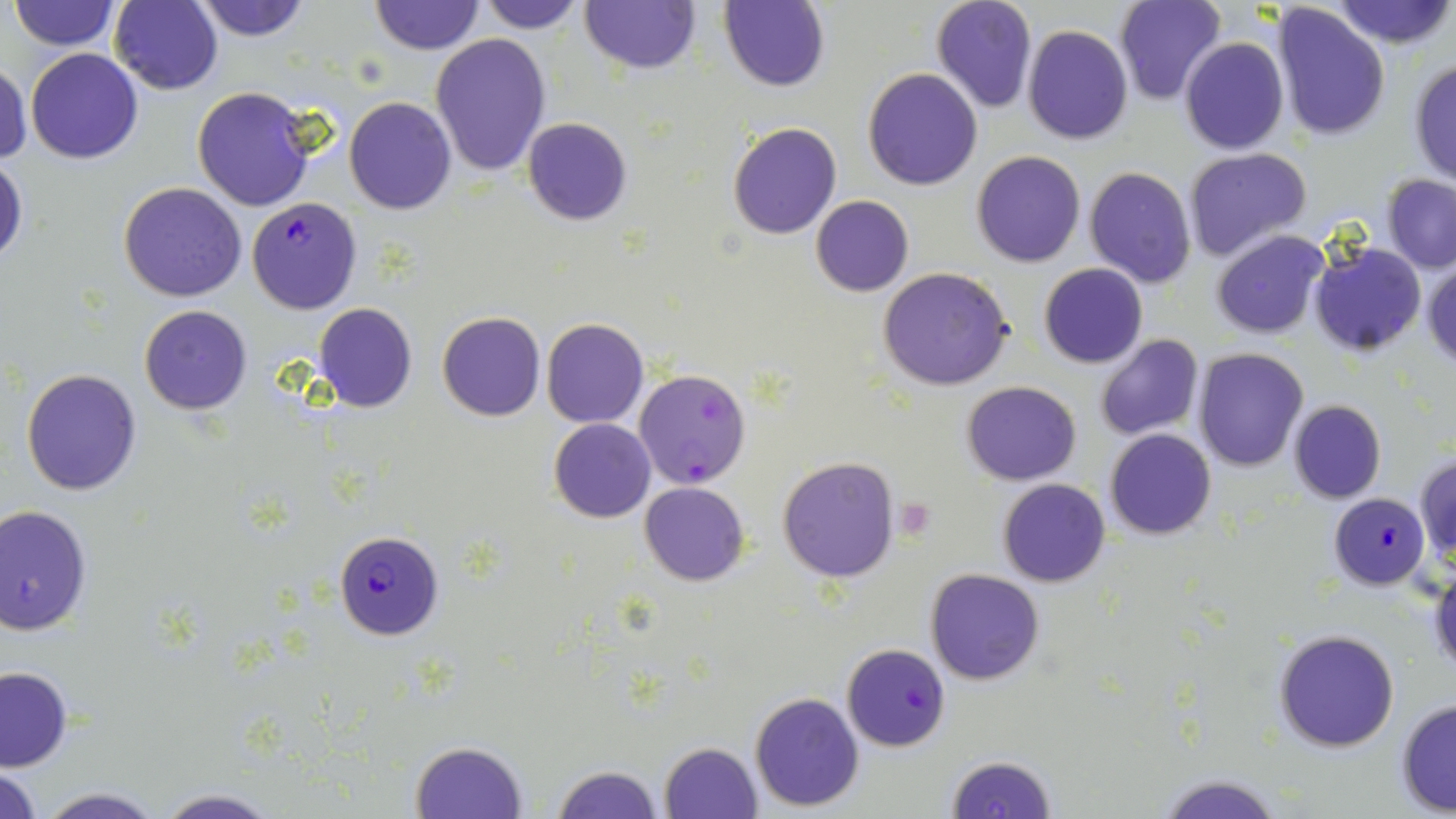
Approximate bounding boxes as (x1,y1)-(x2,y2) corner pairs in pixels. Plasmodium falciparum-infected red blood cell locations: (246,197)-(362,315), (633,368)-(751,490), (1329,492)-(1430,590), (334,531)-(443,640), (842,643)-(951,751). Platelet locations: (895,497)-(935,540). Uninfected red blood cell locations: (191,0)-(315,41), (580,0)-(700,73), (932,0)-(1038,114), (1115,0)-(1225,108), (1331,0)-(1456,50), (9,1)-(121,51), (109,1)-(222,94), (476,1)-(587,33), (720,1)-(830,91), (368,2)-(485,54), (1271,3)-(1392,142), (1022,23)-(1133,147), (429,34)-(550,178), (1180,36)-(1288,156), (25,48)-(144,163), (0,57)-(32,168), (1408,59)-(1456,187), (863,67)-(982,190), (190,85)-(317,213), (342,95)-(457,215), (522,117)-(633,226), (727,121)-(842,240), (1182,146)-(1313,262), (971,151)-(1085,268), (0,156)-(27,269), (1082,166)-(1198,289), (1383,173)-(1456,274), (118,182)-(248,302), (810,194)-(913,296), (1211,230)-(1328,340), (1307,241)-(1428,357), (1423,260)-(1456,369), (1038,262)-(1147,368), (878,268)-(1015,392), (312,302)-(418,413), (139,305)-(252,415), (436,312)-(546,422), (541,318)-(649,428), (1095,334)-(1204,442), (1192,348)-(1309,471), (21,369)-(143,496), (962,381)-(1081,485), (1287,399)-(1387,503), (548,418)-(656,523), (1105,429)-(1217,540), (1416,452)-(1456,571), (776,455)-(902,582), (997,478)-(1109,587), (639,481)-(749,585), (0,504)-(95,635), (1429,566)-(1456,675), (924,568)-(1045,686), (1272,629)-(1399,752), (0,666)-(73,772), (750,692)-(864,809), (1395,699)-(1456,815), (410,741)-(527,818), (658,741)-(763,819), (945,754)-(1058,819), (0,764)-(42,818), (550,764)-(664,819), (1156,774)-(1286,818), (36,786)-(165,818), (153,789)-(281,819). Slide-level diagnosis: Plasmodium falciparum. Captured at 1000x magnification. Thin blood smear. One field of a larger specimen. Image is 1456×819 pixels. Optical microscopy. May-Grünwald-Giemsa-stained preparation.